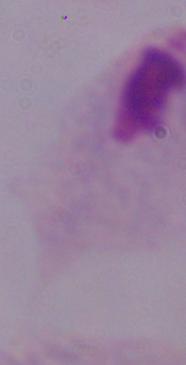
{
  "modality": "micrograph",
  "identification": "trichomonad",
  "magnification": "1000x"
}